Locate every uninfected red blood cell.
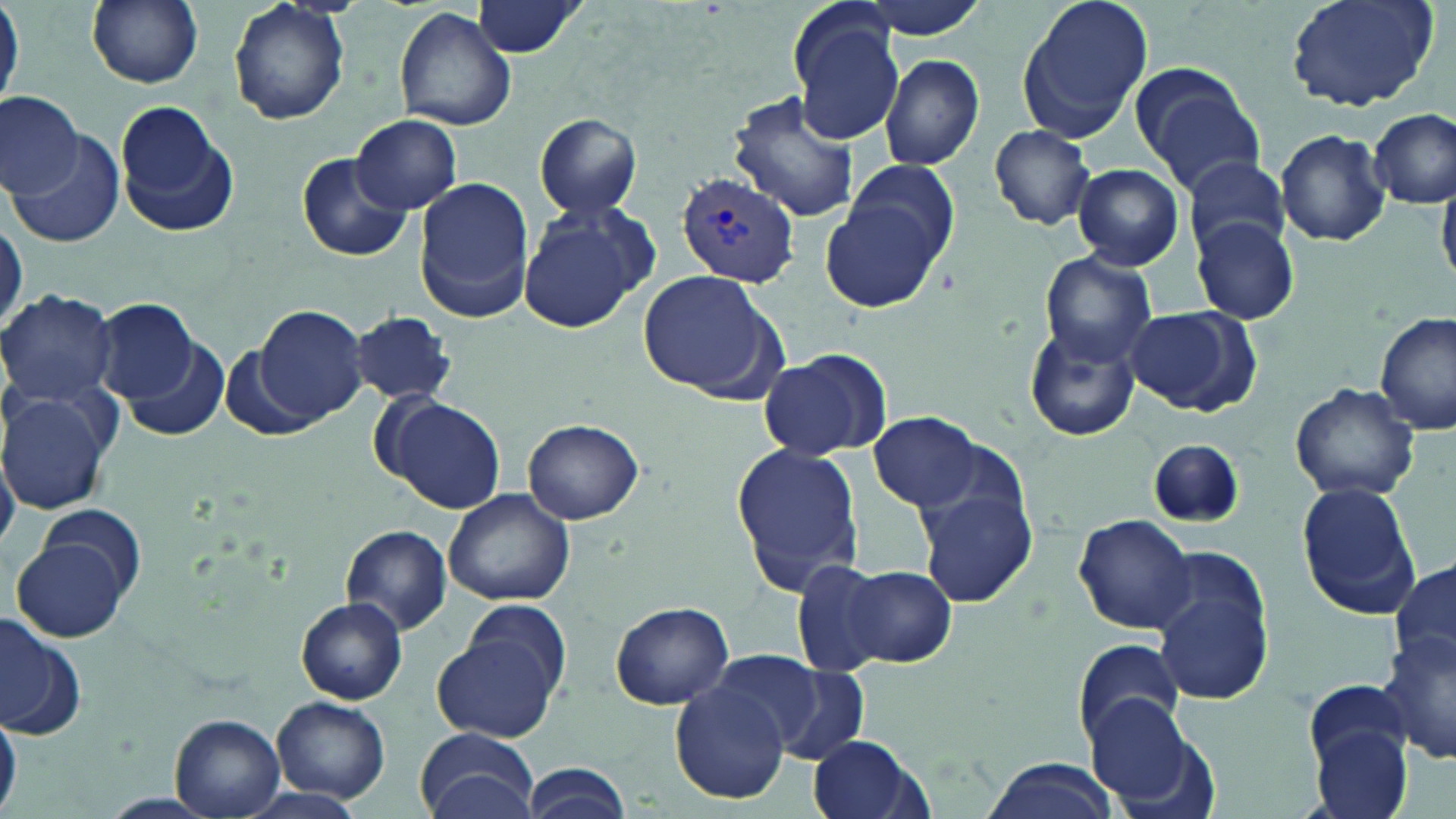

Approximate bounding boxes as [x1, y1, x2, y2] in pixels.
Uninfected red blood cells: [0, 0, 22, 114], [86, 0, 205, 88], [228, 0, 352, 126], [855, 0, 993, 40], [1015, 0, 1155, 145], [1282, 0, 1439, 113], [469, 2, 587, 57], [788, 3, 907, 145], [393, 6, 518, 134], [880, 54, 985, 171], [1134, 70, 1266, 197], [0, 93, 81, 197], [729, 94, 860, 223], [113, 105, 237, 237], [1370, 109, 1454, 208], [533, 111, 643, 219], [351, 115, 462, 213], [989, 124, 1095, 230], [1277, 129, 1391, 247], [11, 132, 125, 250], [298, 150, 412, 262], [1184, 155, 1291, 257], [842, 159, 958, 267], [1073, 163, 1184, 272], [414, 177, 536, 322], [823, 197, 946, 313], [517, 199, 657, 333], [0, 212, 26, 337], [1190, 216, 1301, 325], [1038, 252, 1158, 367], [639, 268, 780, 400], [0, 289, 118, 408], [94, 297, 199, 402], [252, 304, 372, 426], [1124, 306, 1255, 415], [351, 310, 454, 405], [1376, 313, 1456, 435], [1023, 325, 1141, 443], [121, 332, 228, 440], [759, 348, 892, 463], [218, 349, 317, 442], [1288, 382, 1420, 503], [0, 387, 117, 517], [379, 395, 507, 515], [868, 414, 986, 511], [521, 417, 645, 525], [1146, 439, 1246, 529], [729, 440, 868, 596], [1294, 481, 1422, 618], [916, 486, 1037, 607], [442, 488, 576, 606], [39, 505, 146, 604], [1074, 514, 1196, 635], [341, 523, 451, 637], [14, 534, 130, 642], [791, 559, 890, 679], [1390, 559, 1456, 675], [842, 565, 953, 666], [1152, 579, 1274, 705], [297, 599, 407, 704], [607, 600, 732, 711], [455, 601, 575, 707], [0, 612, 84, 740], [433, 631, 562, 743], [1382, 632, 1456, 764], [1073, 640, 1183, 743], [709, 651, 832, 749], [769, 664, 868, 764], [1306, 680, 1409, 769], [670, 682, 789, 804], [273, 695, 391, 803], [1086, 698, 1208, 814], [0, 703, 21, 818], [169, 713, 284, 818], [415, 728, 540, 819], [1310, 728, 1415, 819], [809, 735, 931, 819], [979, 757, 1121, 819], [519, 762, 632, 819].

Plasmodium vivax-infected red blood cell locations: [675, 171, 801, 286]. Slide-level diagnosis: Plasmodium vivax. Image is 1456×819 pixels. Thin blood smear. Captured at 1000x magnification. May-Grünwald-Giemsa-stained preparation. Light microscopy. One field of a larger specimen.